Report the malaria status of this cell.
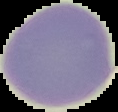

Uninfected.

preparation = thin blood film
image type = segmented cell region with the area outside set to black
image size = 118×112 pixels